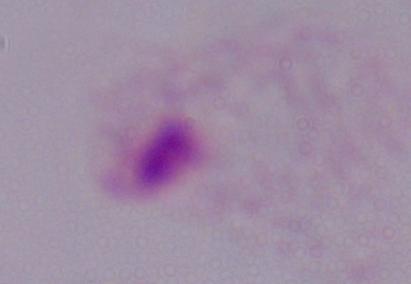
identification = trichomonad
modality = micrograph
magnification = 1000x